Locate the P. falciparum-infected red blood cells and any of indeterminate infection status.
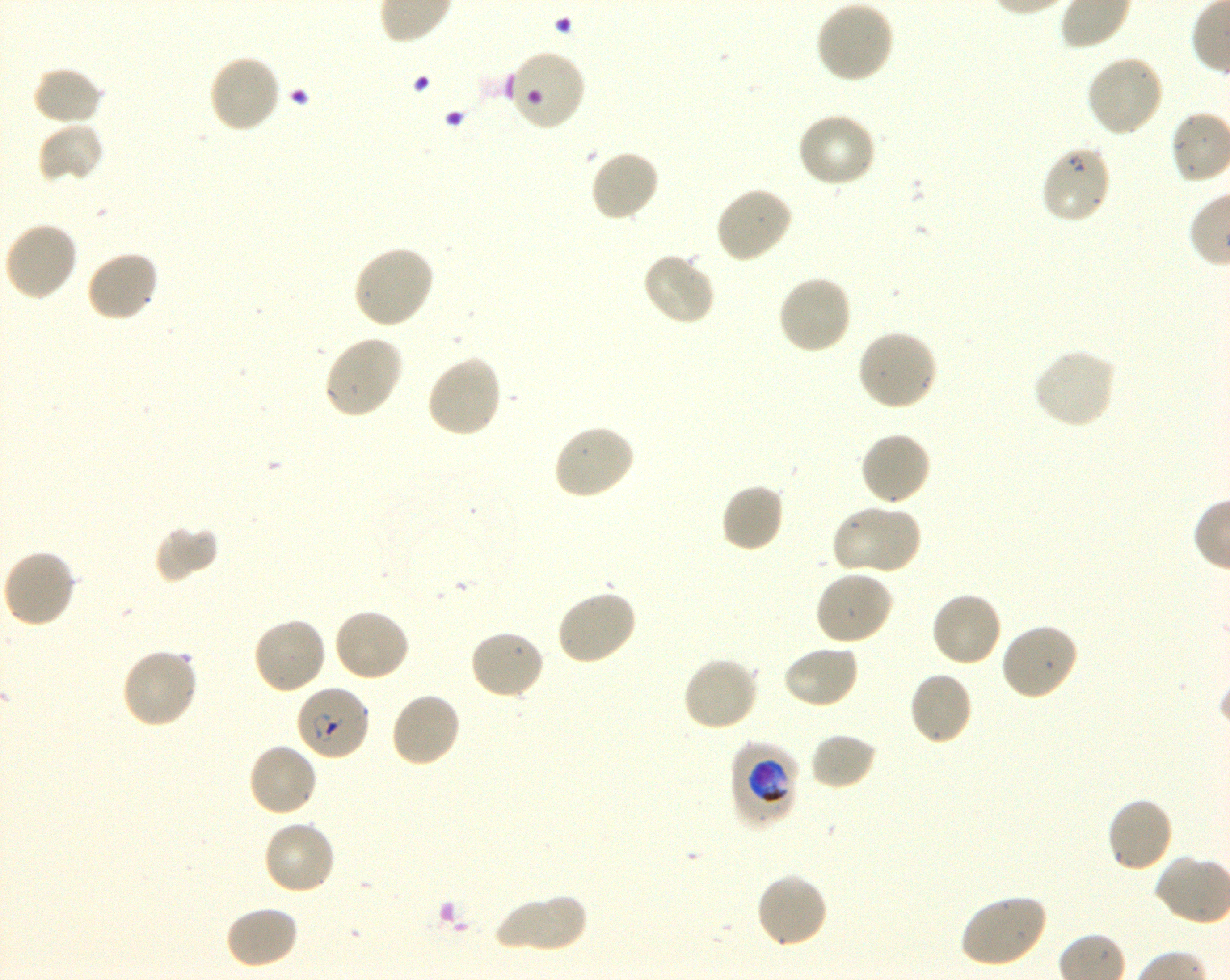

Approximate bounding rectangles given as corner coordinates in pixels from the top-left. Not every red blood cell is marked. A life-cycle stage — or a range of stages, where the recorded stages span more than one — follows each staged infected red blood cell.
Infected red blood cells: (x1=1039, y1=144, x2=1112, y2=225); (x1=295, y1=683, x2=371, y2=761) ring; (x1=729, y1=741, x2=801, y2=829) trophozoite.
Red blood cells of indeterminate infection status: (x1=505, y1=47, x2=587, y2=133).

Summary:
  - Locations of uninfected red blood cells: (x1=815, y1=0, x2=895, y2=84), (x1=206, y1=52, x2=282, y2=135), (x1=1085, y1=53, x2=1165, y2=139), (x1=31, y1=66, x2=105, y2=127), (x1=796, y1=112, x2=877, y2=190), (x1=36, y1=121, x2=105, y2=185), (x1=588, y1=149, x2=660, y2=223), (x1=714, y1=185, x2=793, y2=264), (x1=2, y1=220, x2=79, y2=302), (x1=351, y1=244, x2=436, y2=330), (x1=85, y1=249, x2=161, y2=323), (x1=641, y1=251, x2=717, y2=327), (x1=776, y1=275, x2=853, y2=356), (x1=855, y1=328, x2=939, y2=413), (x1=322, y1=334, x2=404, y2=420), (x1=1031, y1=346, x2=1117, y2=430), (x1=425, y1=354, x2=504, y2=439), (x1=551, y1=423, x2=635, y2=501), (x1=859, y1=431, x2=932, y2=507), (x1=720, y1=482, x2=785, y2=553), (x1=830, y1=504, x2=922, y2=577), (x1=153, y1=524, x2=219, y2=584), (x1=1, y1=548, x2=77, y2=629), (x1=814, y1=569, x2=894, y2=647), (x1=556, y1=588, x2=638, y2=666), (x1=931, y1=591, x2=1003, y2=668), (x1=332, y1=607, x2=412, y2=683), (x1=252, y1=616, x2=329, y2=695), (x1=998, y1=621, x2=1079, y2=702), (x1=467, y1=628, x2=546, y2=701), (x1=781, y1=643, x2=860, y2=710), (x1=120, y1=648, x2=200, y2=730), (x1=682, y1=655, x2=761, y2=732), (x1=908, y1=671, x2=973, y2=747), (x1=389, y1=690, x2=462, y2=769), (x1=809, y1=731, x2=879, y2=790), (x1=246, y1=741, x2=319, y2=818), (x1=1105, y1=797, x2=1175, y2=873), (x1=262, y1=819, x2=337, y2=896), (x1=754, y1=872, x2=829, y2=949), (x1=493, y1=893, x2=590, y2=953), (x1=957, y1=893, x2=1048, y2=968), (x1=224, y1=904, x2=299, y2=969)
  - Life-cycle stages observed: ring, trophozoite
  - Preparation: thin blood smear
  - Stain: Giemsa
  - Donor blood group: O+
  - Objective: 100x, oil immersion, numerical aperture 1.30
  - Field of view: one from this slide
  - Culture: P. falciparum strain 3D7, shaking, in vitro
  - Image size: 1230×980 pixels